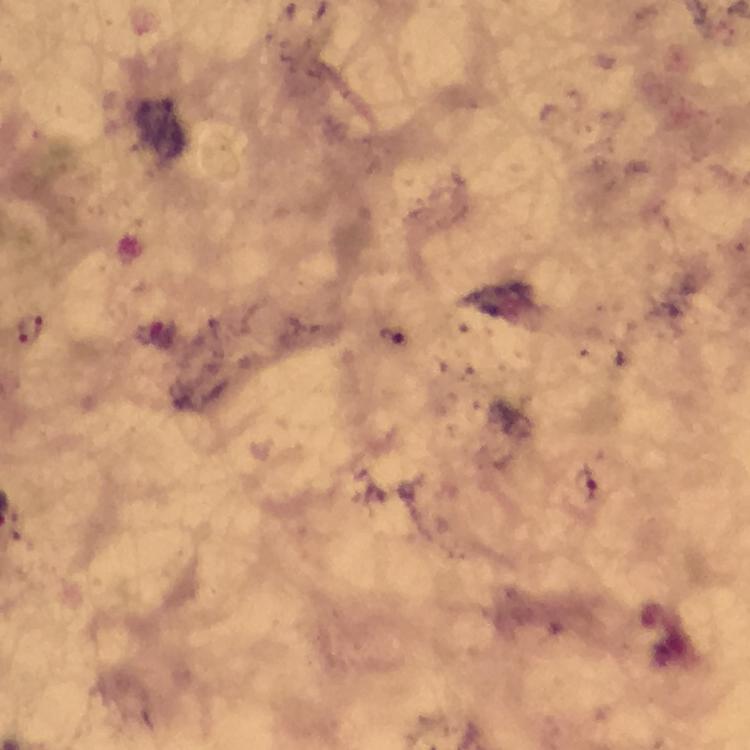
Approximate centers as [x, y] in pixels. Plasmodium parasite locations: [28, 327], [390, 334], [586, 486]. Thick blood smear. Giemsa-stained preparation. Smartphone photograph taken through a microscope. Cropped region of a single field of view. Image is 750×750 pixels. Immersion oil was used. 100x magnification. From a malaria diagnostic workup.